Evaluate for Plasmodium parasites.
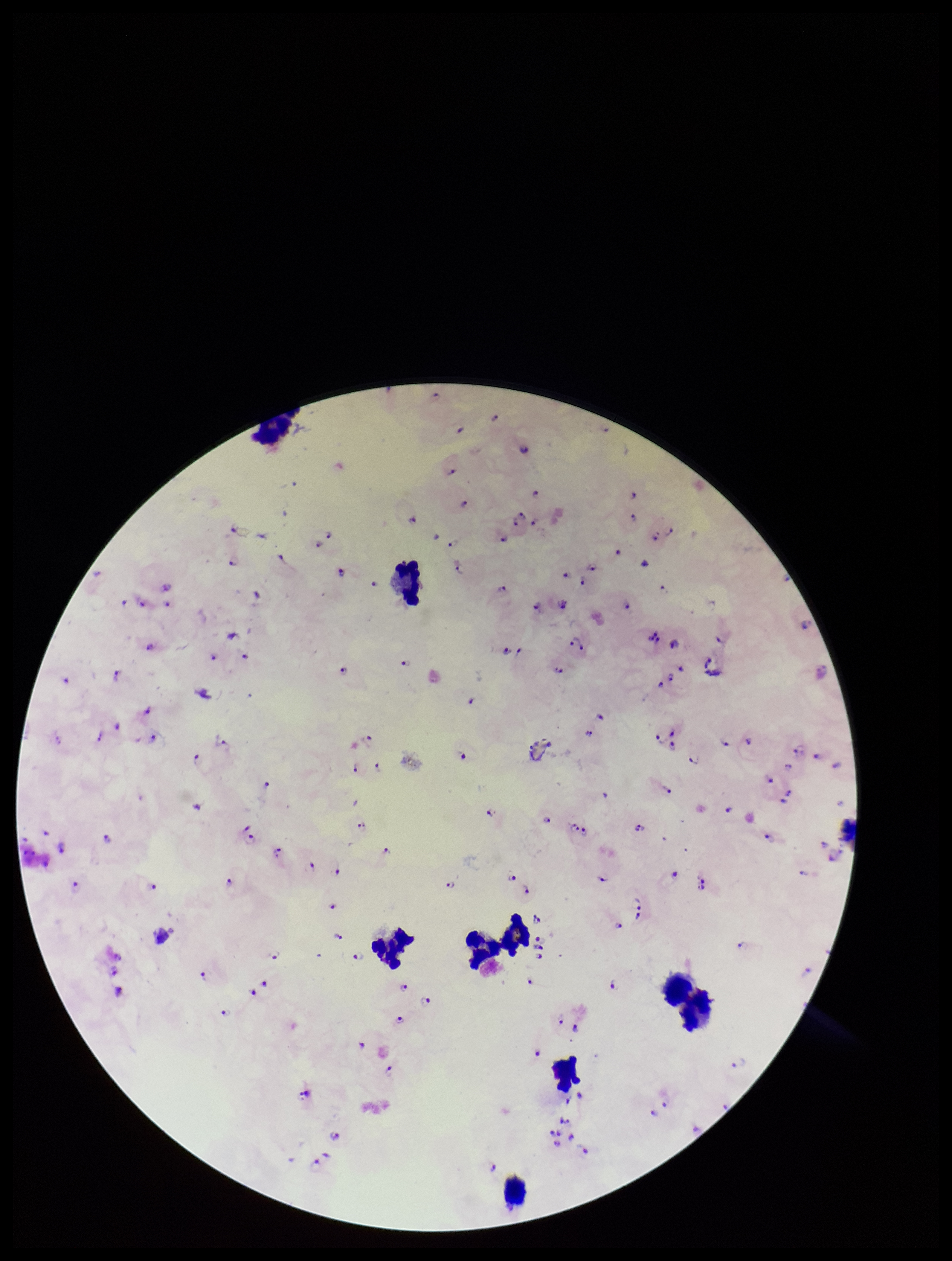

Seen.

Summary:
  - Stain: Giemsa
  - Species reported for this patient: Plasmodium falciparum
  - Field of view: single
  - Capture: smartphone photograph through the microscope eyepiece
  - Preparation: thick smear
  - Leukocyte count: 9
  - Patient malaria status: infected
  - Image size: 952×1261 pixels
  - Parasite count: 97